Locate and identify every blood parasite.
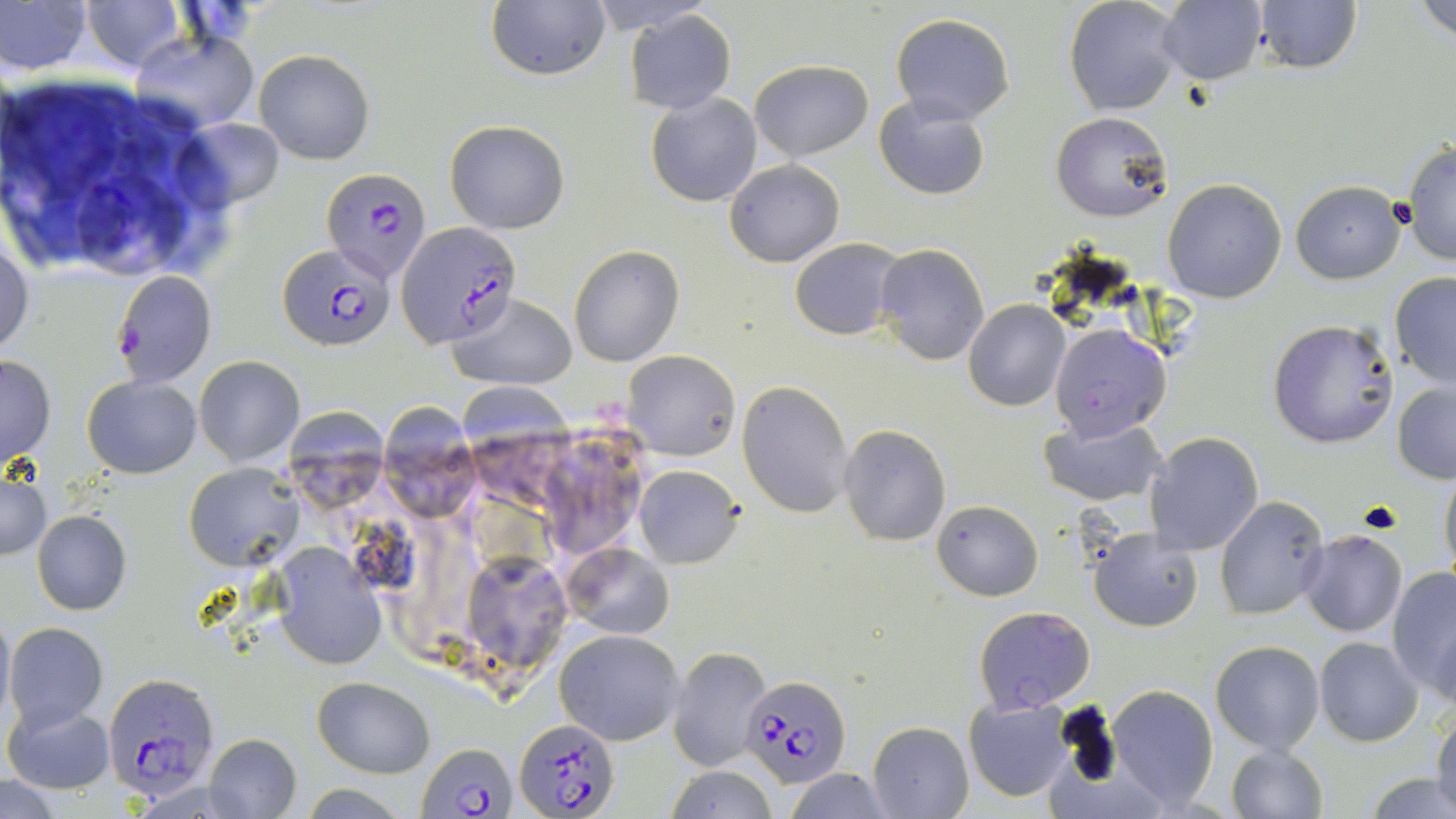
Approximate bounding boxes as [x1, y1, x2, y2] in pixels.
Plasmodium falciparum-infected red blood cells: [321, 166, 431, 280], [396, 220, 520, 349], [278, 243, 397, 352], [113, 271, 216, 387], [103, 674, 222, 797], [740, 674, 848, 788], [516, 718, 619, 819], [417, 741, 517, 819].
No Plasmodium ovale, Plasmodium malariae, Plasmodium vivax, Babesia divergens, or Trypanosoma brucei observed.

Summary:
  - White blood cell locations: [3, 77, 243, 282]
  - Uninfected red blood cell locations: [80, 0, 184, 73], [1064, 0, 1185, 117], [1414, 0, 1456, 42], [486, 1, 611, 83], [1252, 1, 1362, 73], [0, 2, 91, 76], [1158, 2, 1267, 84], [625, 9, 737, 113], [890, 13, 1015, 125], [131, 30, 259, 131], [255, 49, 375, 163], [749, 59, 873, 162], [646, 92, 762, 206], [874, 94, 993, 200], [1050, 111, 1172, 223], [179, 118, 286, 212], [445, 119, 570, 233], [1404, 142, 1456, 265], [724, 159, 844, 266], [1162, 178, 1287, 303], [1291, 179, 1405, 284], [0, 234, 35, 357], [789, 238, 904, 340], [569, 244, 683, 367], [873, 244, 989, 365], [1389, 272, 1456, 387], [450, 293, 576, 389], [963, 301, 1069, 412], [1267, 319, 1399, 449], [1049, 323, 1172, 444], [622, 350, 741, 460], [0, 353, 56, 466], [194, 355, 304, 466], [82, 374, 201, 478], [462, 375, 565, 499], [1391, 380, 1455, 484], [737, 381, 853, 517], [386, 395, 479, 517], [288, 409, 383, 509], [1039, 415, 1166, 507], [839, 424, 951, 546], [1146, 432, 1263, 556], [549, 433, 647, 554], [1439, 462, 1456, 590], [184, 463, 300, 570], [632, 463, 744, 568], [1, 469, 49, 560], [1214, 496, 1329, 621], [933, 499, 1043, 600], [32, 510, 132, 614], [1087, 528, 1203, 631], [1298, 529, 1408, 637], [273, 545, 390, 670], [565, 546, 674, 640], [470, 555, 566, 666], [1387, 565, 1456, 699], [972, 606, 1094, 713], [0, 607, 13, 727], [4, 621, 108, 728], [555, 630, 684, 745], [1315, 637, 1423, 746], [1210, 639, 1325, 754], [667, 645, 771, 771], [314, 677, 434, 778], [1106, 684, 1219, 810], [964, 697, 1075, 802], [3, 701, 114, 796], [1433, 710, 1456, 811], [867, 721, 974, 818], [203, 733, 301, 819], [1226, 744, 1328, 819], [665, 764, 778, 819], [784, 768, 893, 819], [1366, 773, 1456, 819], [0, 777, 71, 818]
  - Slide-level diagnosis: Plasmodium falciparum
  - Magnification: 1000x
  - Stain: May-Grünwald-Giemsa
  - Image size: 1456×819 pixels
  - Modality: light microscopy
  - Field of view: one of a larger specimen
  - Preparation: thin blood smear